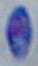

magnification = 1000x
identification = Toxoplasma gondii
modality = micrograph